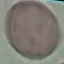
result = no malaria parasites seen
capture = smartphone through the microscope eyepiece
image type = cell patch, automatically extracted from a larger field of view and resized to 64 × 64 pixels
stain = Giemsa
preparation = thin blood smear